Give the preparation type.
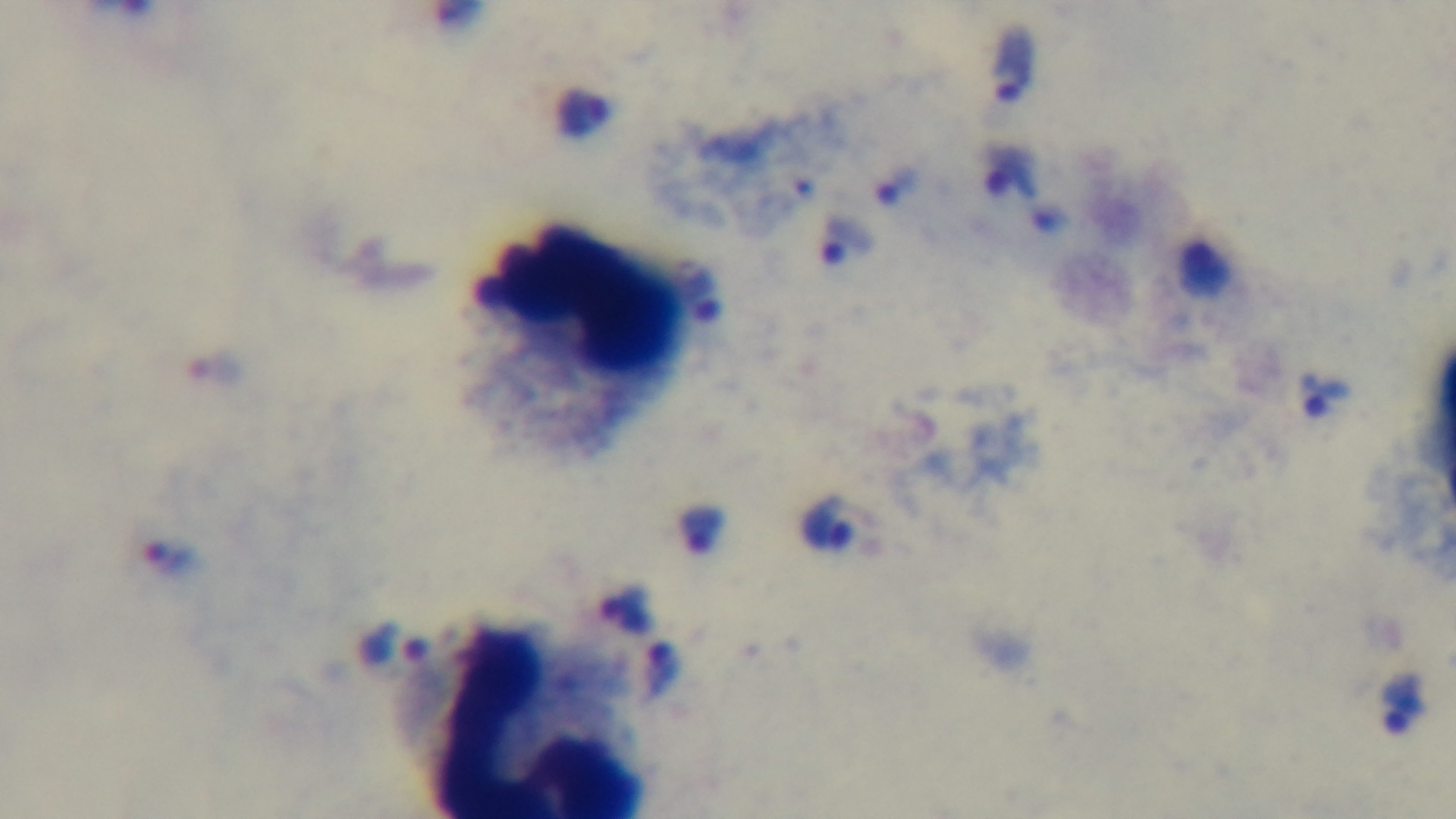
It is a thick blood film.

Summary:
  - Modality: light microscopy
  - Stain: Giemsa
  - Objective: 100x oil immersion
  - Malaria status: infected
  - Capture: mounted 4K digital camera
  - Field of view: one from the slide